Give the position of every Plasmodium parasite visible.
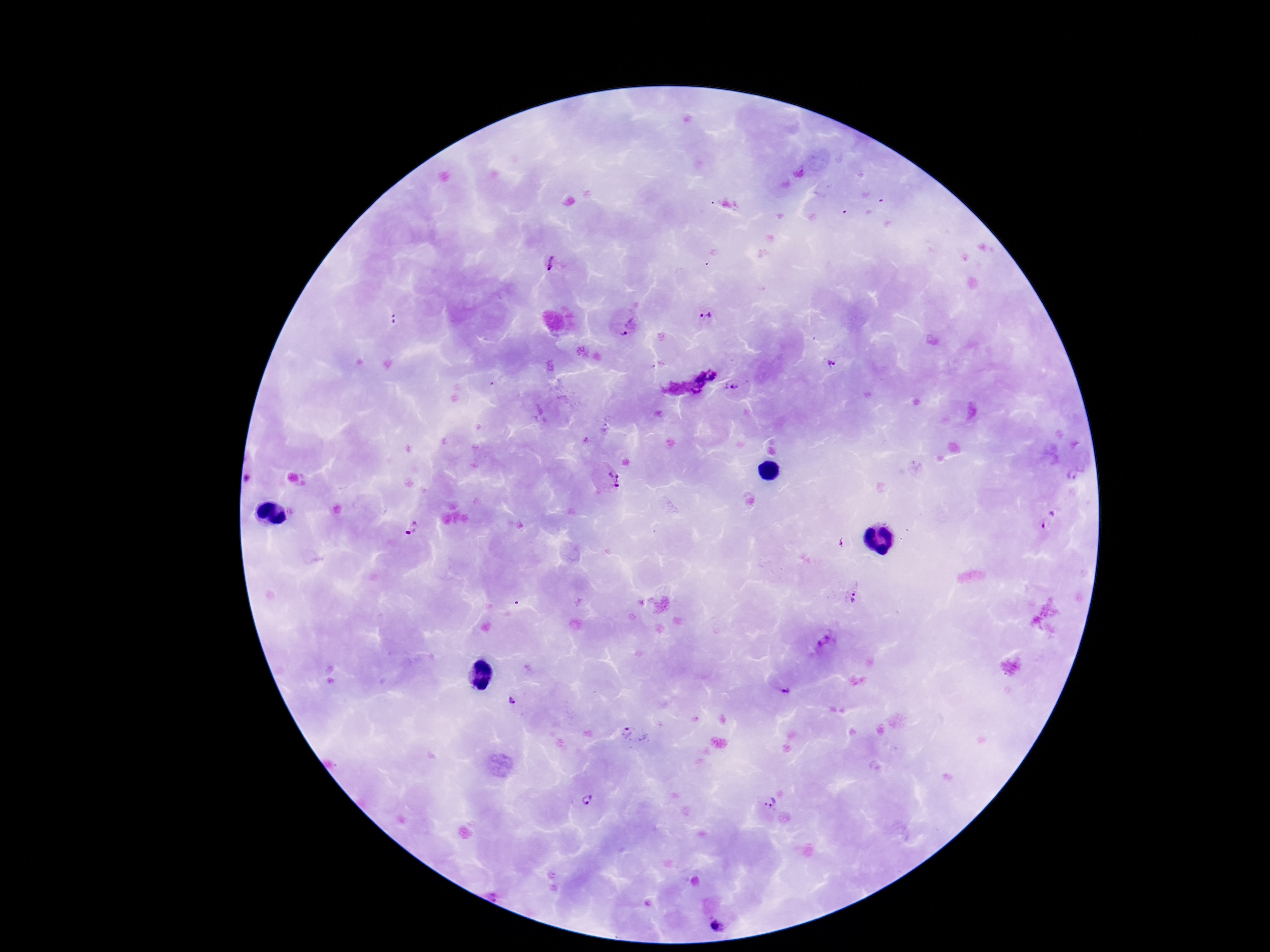

Approximate centers as [x, y] in pixels.
Plasmodium parasites: [552, 262], [705, 317], [394, 321], [625, 336], [832, 365], [706, 377], [733, 388], [614, 478], [248, 481], [1048, 521], [411, 531], [854, 597], [825, 642], [785, 689], [512, 701], [636, 737], [587, 799], [770, 802], [716, 927].

field_of_view: one from this slide
preparation: thick blood smear
image_size: 1270×952 pixels
capture: smartphone camera through the microscope eyepiece
stain: Giemsa
patient_malaria_status: infected
magnification: 100x